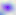

{
  "magnification": "400x",
  "identification": "Toxoplasma gondii",
  "modality": "micrograph"
}